Point out each leukocyte.
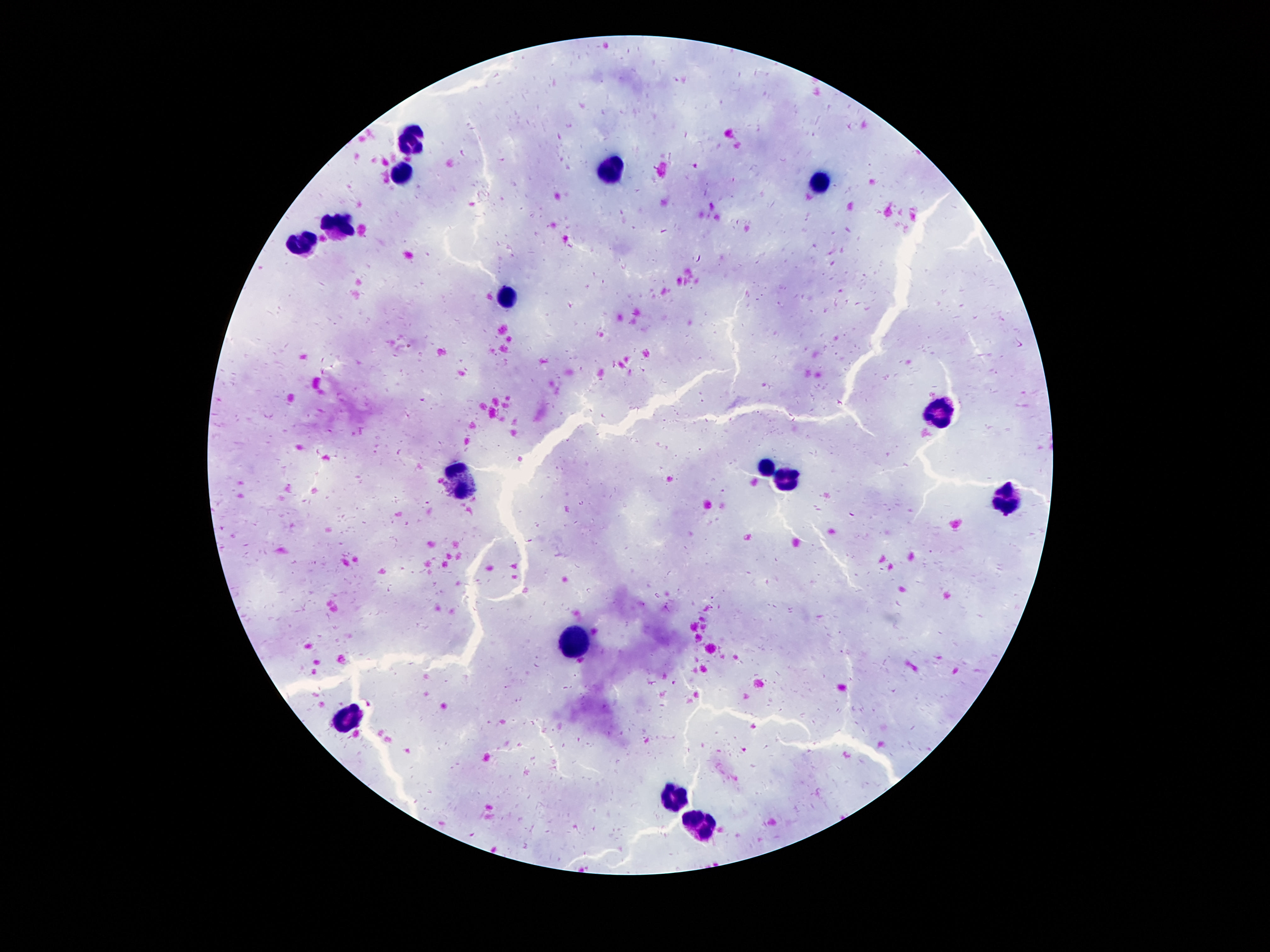
Approximate centers as [x, y] in pixels.
Leukocytes: [409, 134], [614, 172], [402, 173], [820, 183], [334, 227], [300, 241], [507, 298], [942, 411], [765, 465], [788, 479], [462, 482], [1004, 497], [568, 642], [352, 721], [675, 793], [698, 829].

100x magnification. Photographed through the microscope eyepiece with a smartphone camera. Thick peripheral-blood smear. One field from this slide. Image is 1270×952 pixels. Patient malaria status: negative. Giemsa-stained preparation.